State the blood parasite species.
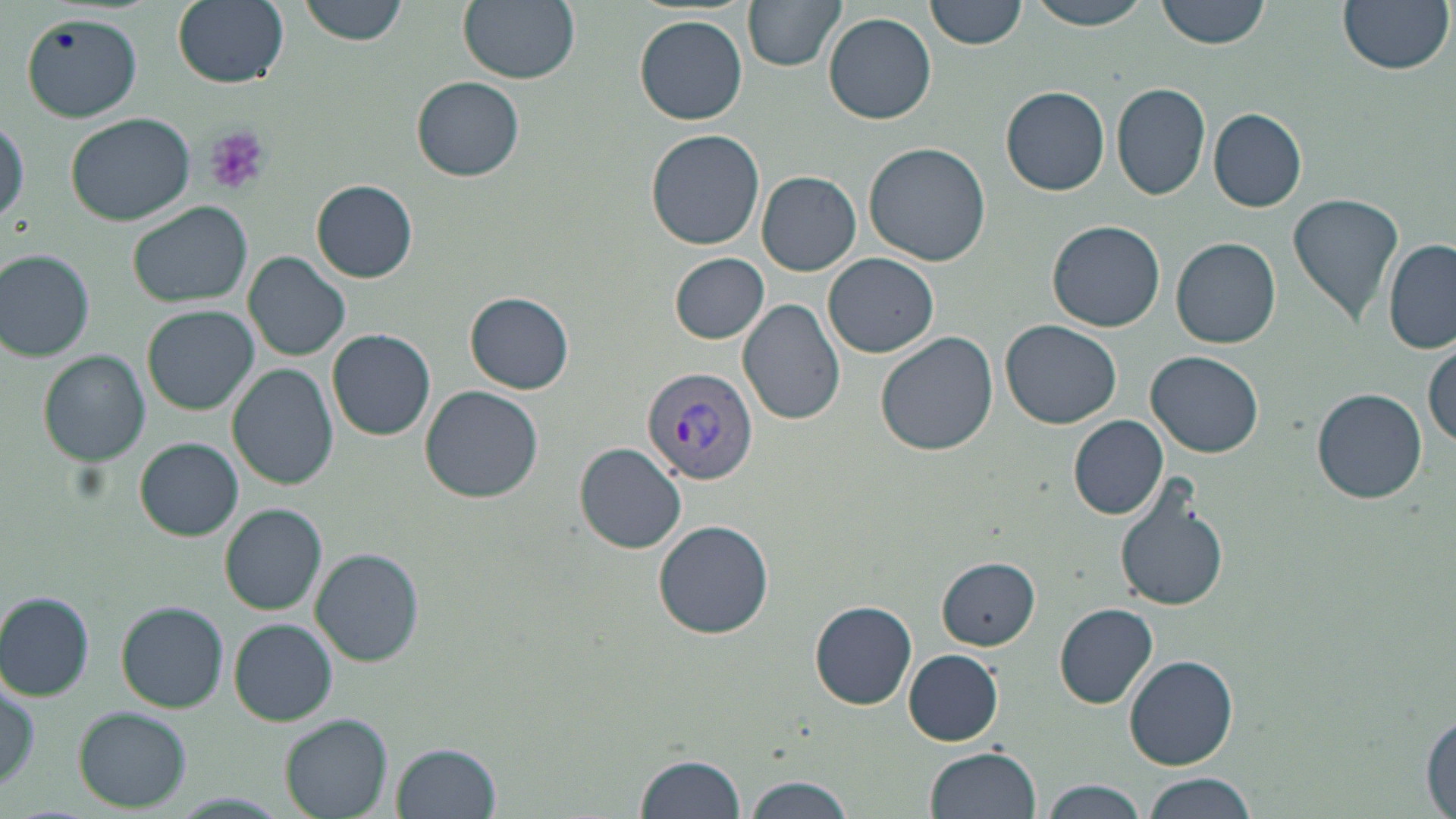
Plasmodium vivax.

stain = May-Grünwald-Giemsa
platelet locations = approximate bounding boxes as named x1/y1/x2/y2 corners in pixels: (x1=206, y1=126, x2=272, y2=198)
field of view = one of a larger specimen
preparation = thin blood film
image size = 1456×819 pixels
Plasmodium vivax-infected red blood cell locations = approximate bounding boxes as named x1/y1/x2/y2 corners in pixels: (x1=642, y1=366, x2=760, y2=486)
magnification = 1000x
uninfected red blood cell locations = approximate bounding boxes as named x1/y1/x2/y2 corners in pixels: (x1=171, y1=0, x2=289, y2=89), (x1=299, y1=0, x2=409, y2=45), (x1=458, y1=0, x2=580, y2=84), (x1=745, y1=0, x2=845, y2=70), (x1=926, y1=0, x2=1027, y2=50), (x1=1023, y1=0, x2=1154, y2=31), (x1=1157, y1=0, x2=1272, y2=49), (x1=1336, y1=0, x2=1452, y2=74), (x1=825, y1=12, x2=936, y2=124), (x1=21, y1=14, x2=143, y2=122), (x1=634, y1=15, x2=749, y2=125), (x1=413, y1=76, x2=524, y2=181), (x1=1111, y1=82, x2=1210, y2=200), (x1=1002, y1=86, x2=1110, y2=196), (x1=1209, y1=108, x2=1307, y2=212), (x1=66, y1=111, x2=195, y2=225), (x1=1, y1=116, x2=29, y2=227), (x1=646, y1=130, x2=765, y2=249), (x1=863, y1=141, x2=992, y2=265), (x1=756, y1=171, x2=861, y2=276), (x1=311, y1=180, x2=418, y2=282), (x1=1287, y1=192, x2=1405, y2=328), (x1=129, y1=200, x2=253, y2=307), (x1=1046, y1=219, x2=1166, y2=332), (x1=1171, y1=237, x2=1280, y2=348), (x1=1385, y1=241, x2=1456, y2=354), (x1=1, y1=250, x2=97, y2=361), (x1=244, y1=252, x2=350, y2=360), (x1=669, y1=253, x2=769, y2=344), (x1=824, y1=253, x2=939, y2=358), (x1=465, y1=292, x2=574, y2=394), (x1=738, y1=298, x2=847, y2=426), (x1=144, y1=306, x2=258, y2=414), (x1=1000, y1=321, x2=1123, y2=429), (x1=328, y1=329, x2=436, y2=439), (x1=877, y1=333, x2=999, y2=458), (x1=1425, y1=339, x2=1456, y2=449), (x1=1146, y1=350, x2=1265, y2=457), (x1=41, y1=351, x2=151, y2=466), (x1=228, y1=365, x2=338, y2=491), (x1=421, y1=386, x2=544, y2=503), (x1=1312, y1=389, x2=1428, y2=504), (x1=1069, y1=417, x2=1167, y2=519), (x1=135, y1=439, x2=243, y2=539), (x1=576, y1=442, x2=687, y2=554), (x1=1113, y1=480, x2=1230, y2=612), (x1=222, y1=504, x2=327, y2=614), (x1=653, y1=520, x2=776, y2=639), (x1=310, y1=548, x2=425, y2=665), (x1=937, y1=556, x2=1041, y2=650), (x1=0, y1=593, x2=95, y2=700), (x1=810, y1=600, x2=916, y2=709), (x1=118, y1=603, x2=229, y2=712), (x1=1054, y1=603, x2=1159, y2=709), (x1=230, y1=619, x2=336, y2=726), (x1=903, y1=649, x2=1004, y2=746), (x1=1125, y1=656, x2=1239, y2=768), (x1=2, y1=678, x2=39, y2=799), (x1=76, y1=708, x2=191, y2=811), (x1=1421, y1=711, x2=1455, y2=815), (x1=280, y1=714, x2=391, y2=819), (x1=390, y1=741, x2=501, y2=818), (x1=925, y1=747, x2=1041, y2=819), (x1=634, y1=753, x2=746, y2=819), (x1=1141, y1=773, x2=1257, y2=819), (x1=741, y1=777, x2=856, y2=819), (x1=1041, y1=780, x2=1152, y2=819), (x1=172, y1=792, x2=287, y2=816)
modality = optical microscopy